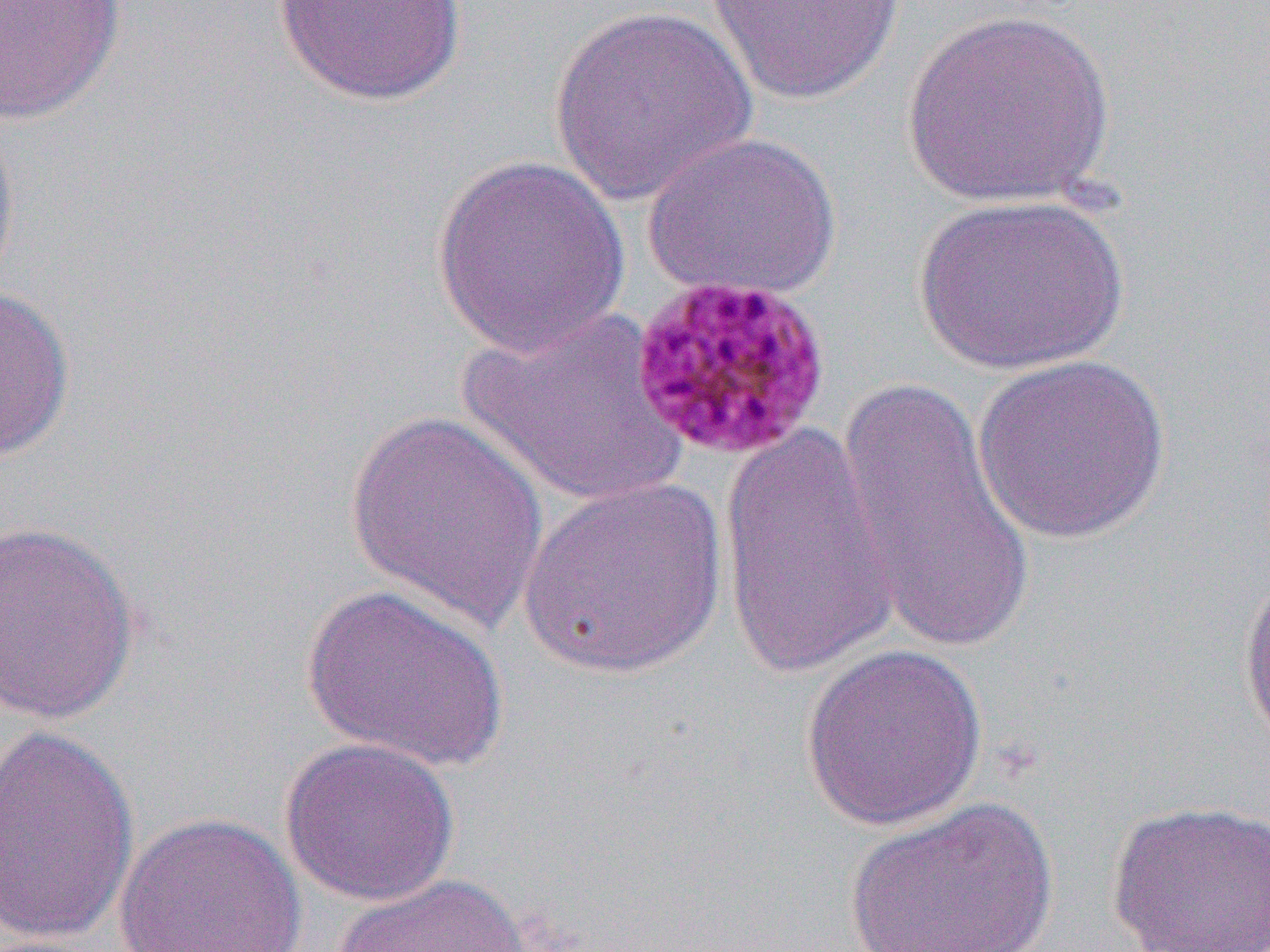
slide_level_diagnosis: Plasmodium malariae
field_of_view: one of a larger specimen
magnification: 1000x
image_size: 1270×952 pixels
uninfected_red_blood_cell_locations: 'approximate bounding boxes as [x1, y1, x2, y2] in pixels: [271, 0, 469, 107], [703, 0, 906, 106], [0, 1, 127, 126], [547, 5, 758, 207], [901, 6, 1117, 209], [0, 110, 22, 297], [642, 131, 843, 303], [430, 153, 630, 360], [915, 193, 1129, 376], [0, 283, 76, 464], [457, 305, 689, 508], [971, 354, 1172, 545], [831, 374, 1037, 653], [343, 410, 553, 633], [717, 419, 901, 685], [515, 475, 731, 680], [0, 519, 141, 726], [1237, 572, 1270, 756], [300, 583, 510, 773], [799, 643, 989, 832], [1, 722, 140, 948], [280, 735, 459, 907], [841, 796, 1060, 952], [1105, 799, 1270, 952], [112, 811, 309, 952], [333, 873, 535, 952]'
modality: light microscopy
preparation: thin blood film